Outline every malaria parasite.
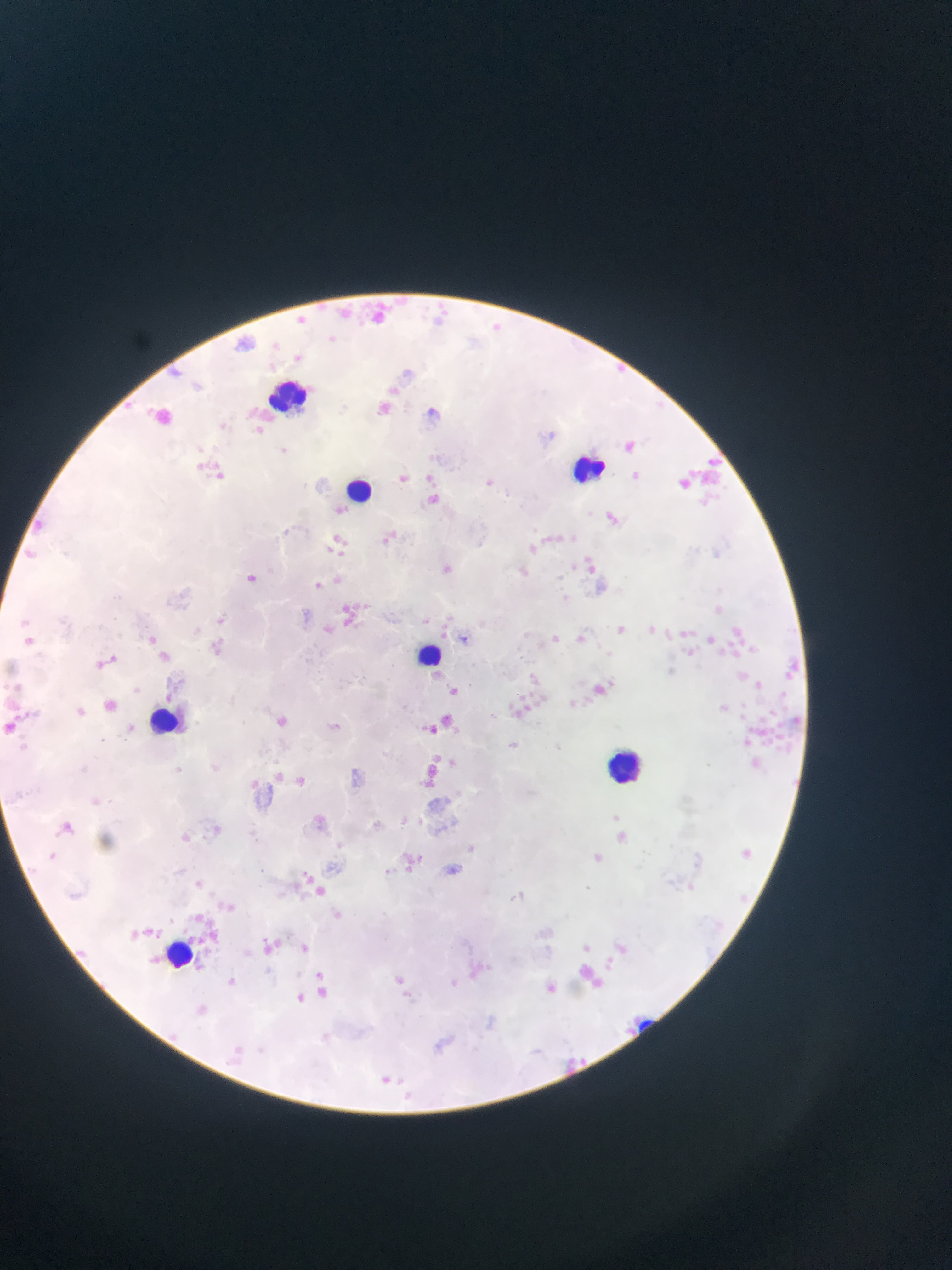

Approximate bounding boxes as [left, top, right, bottom] in pixels.
Malaria parasites: [168, 362, 185, 381], [125, 397, 143, 416], [253, 423, 265, 436], [197, 457, 209, 470], [210, 467, 231, 485], [631, 469, 645, 487], [424, 470, 440, 489], [395, 471, 412, 484], [484, 479, 499, 492], [606, 505, 623, 526], [25, 517, 47, 535], [380, 529, 394, 541], [340, 537, 359, 555], [323, 539, 337, 555], [529, 539, 541, 560], [443, 559, 456, 576], [589, 563, 600, 578], [339, 569, 350, 582], [247, 572, 261, 581], [314, 572, 325, 589], [214, 614, 225, 630], [20, 617, 31, 627], [617, 623, 627, 646], [572, 625, 586, 647], [149, 631, 163, 646], [551, 631, 565, 645], [24, 635, 35, 645], [210, 639, 223, 656], [159, 649, 173, 665], [97, 655, 115, 667], [610, 678, 618, 686], [130, 680, 144, 696], [444, 683, 463, 696], [519, 690, 535, 701], [540, 694, 553, 706], [505, 699, 519, 713], [279, 710, 292, 725], [14, 711, 33, 725], [430, 719, 438, 733], [431, 753, 448, 769], [271, 766, 286, 779], [296, 773, 308, 789], [247, 775, 265, 796], [417, 780, 439, 794], [610, 813, 621, 823], [49, 851, 58, 859], [590, 852, 608, 863], [291, 874, 307, 896], [195, 876, 212, 892], [309, 886, 339, 900], [333, 906, 351, 920], [194, 912, 205, 922], [144, 924, 163, 933], [121, 928, 145, 938], [271, 934, 293, 949], [614, 940, 631, 960], [256, 941, 274, 957], [72, 943, 106, 959], [301, 943, 309, 953], [311, 971, 332, 979], [229, 973, 242, 983], [396, 973, 416, 990], [591, 978, 607, 992], [296, 992, 309, 1006], [578, 1054, 586, 1070], [378, 1069, 395, 1086].

Leukocyte locations: [267, 375, 320, 409], [575, 448, 608, 482], [337, 476, 378, 502], [414, 640, 450, 674], [607, 747, 649, 789], [165, 939, 195, 967]. Mobile-phone photograph taken through the microscope. One field of view. Image is 952×1270 pixels. Sample from Ghana. Thin blood smear.